Locate every Plasmodium falciparum-infected red blood cell.
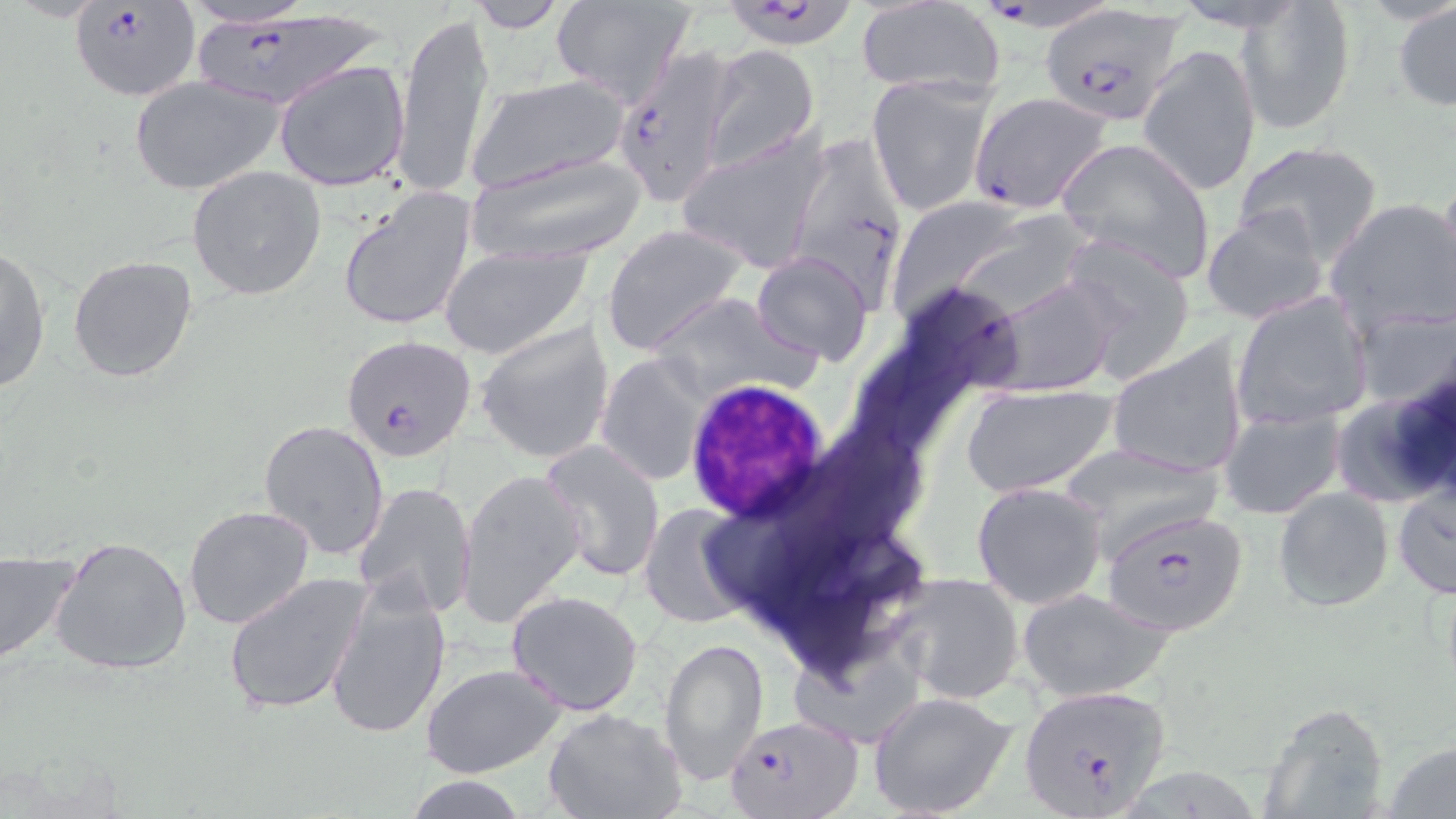

Approximate bounding boxes as named x1/y1/x2/y2 corners in pixels.
Plasmodium falciparum-infected red blood cells: (x1=989, y1=0, x2=1111, y2=33), (x1=68, y1=1, x2=200, y2=101), (x1=717, y1=1, x2=865, y2=49), (x1=1043, y1=6, x2=1183, y2=126), (x1=191, y1=9, x2=390, y2=114), (x1=609, y1=46, x2=740, y2=204), (x1=968, y1=91, x2=1116, y2=213), (x1=801, y1=130, x2=905, y2=318), (x1=340, y1=336, x2=477, y2=462), (x1=1103, y1=508, x2=1248, y2=636), (x1=1017, y1=683, x2=1171, y2=814), (x1=727, y1=714, x2=860, y2=819).

{
  "slide_level_diagnosis": "Plasmodium falciparum",
  "stain": "May-Grünwald-Giemsa",
  "uninfected_red_blood_cell_locations": "approximate bounding boxes as named x1/y1/x2/y2 corners in pixels: (x1=176, y1=0, x2=320, y2=28), (x1=466, y1=0, x2=569, y2=34), (x1=548, y1=1, x2=696, y2=107), (x1=1237, y1=1, x2=1356, y2=135), (x1=1392, y1=1, x2=1456, y2=113), (x1=856, y1=3, x2=1005, y2=94), (x1=394, y1=9, x2=495, y2=197), (x1=1139, y1=45, x2=1260, y2=196), (x1=701, y1=46, x2=820, y2=171), (x1=273, y1=60, x2=410, y2=192), (x1=867, y1=74, x2=999, y2=218), (x1=130, y1=75, x2=283, y2=196), (x1=462, y1=76, x2=635, y2=193), (x1=676, y1=131, x2=832, y2=273), (x1=1055, y1=137, x2=1216, y2=282), (x1=1233, y1=139, x2=1383, y2=264), (x1=459, y1=150, x2=652, y2=269), (x1=186, y1=165, x2=328, y2=301), (x1=1438, y1=166, x2=1456, y2=299), (x1=334, y1=184, x2=479, y2=331), (x1=884, y1=197, x2=1037, y2=318), (x1=1324, y1=197, x2=1456, y2=336), (x1=1200, y1=204, x2=1331, y2=328), (x1=601, y1=225, x2=749, y2=356), (x1=1055, y1=235, x2=1198, y2=378), (x1=437, y1=244, x2=591, y2=358), (x1=1, y1=245, x2=52, y2=394), (x1=751, y1=250, x2=874, y2=366), (x1=67, y1=254, x2=198, y2=383), (x1=988, y1=276, x2=1121, y2=400), (x1=647, y1=290, x2=817, y2=405), (x1=1231, y1=291, x2=1373, y2=429), (x1=1350, y1=306, x2=1456, y2=415), (x1=475, y1=320, x2=615, y2=465), (x1=1106, y1=338, x2=1250, y2=480), (x1=596, y1=352, x2=712, y2=486), (x1=959, y1=383, x2=1119, y2=498), (x1=1330, y1=389, x2=1454, y2=510), (x1=1219, y1=405, x2=1346, y2=520), (x1=257, y1=420, x2=389, y2=561), (x1=538, y1=439, x2=665, y2=582), (x1=1055, y1=443, x2=1223, y2=554), (x1=455, y1=467, x2=588, y2=631), (x1=353, y1=481, x2=478, y2=619), (x1=972, y1=481, x2=1110, y2=609), (x1=1390, y1=483, x2=1455, y2=600), (x1=1273, y1=486, x2=1394, y2=611), (x1=637, y1=502, x2=759, y2=631), (x1=182, y1=504, x2=316, y2=631), (x1=50, y1=535, x2=193, y2=675), (x1=0, y1=548, x2=79, y2=669), (x1=223, y1=570, x2=370, y2=717), (x1=889, y1=574, x2=1024, y2=704), (x1=326, y1=576, x2=453, y2=741), (x1=1018, y1=589, x2=1176, y2=703), (x1=505, y1=590, x2=644, y2=715), (x1=789, y1=634, x2=927, y2=749), (x1=660, y1=635, x2=768, y2=786), (x1=420, y1=663, x2=566, y2=778), (x1=868, y1=690, x2=1018, y2=819), (x1=1257, y1=703, x2=1389, y2=817), (x1=542, y1=709, x2=686, y2=818), (x1=1385, y1=741, x2=1455, y2=819), (x1=406, y1=777, x2=528, y2=818)",
  "white_blood_cell_locations": "approximate bounding boxes as named x1/y1/x2/y2 corners in pixels: (x1=683, y1=378, x2=835, y2=525)",
  "image_size": "1456×819 pixels",
  "field_of_view": "single",
  "magnification": "1000x",
  "modality": "optical microscopy",
  "preparation": "thin blood smear"
}